Report the malaria status of this cell.
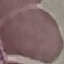
It is uninfected.

Summary:
  - Stain: Giemsa
  - Capture: smartphone camera at the microscope eyepiece
  - Image type: cell patch, automatically extracted from a larger field of view and resized to 64 × 64 pixels
  - Preparation: thin smear